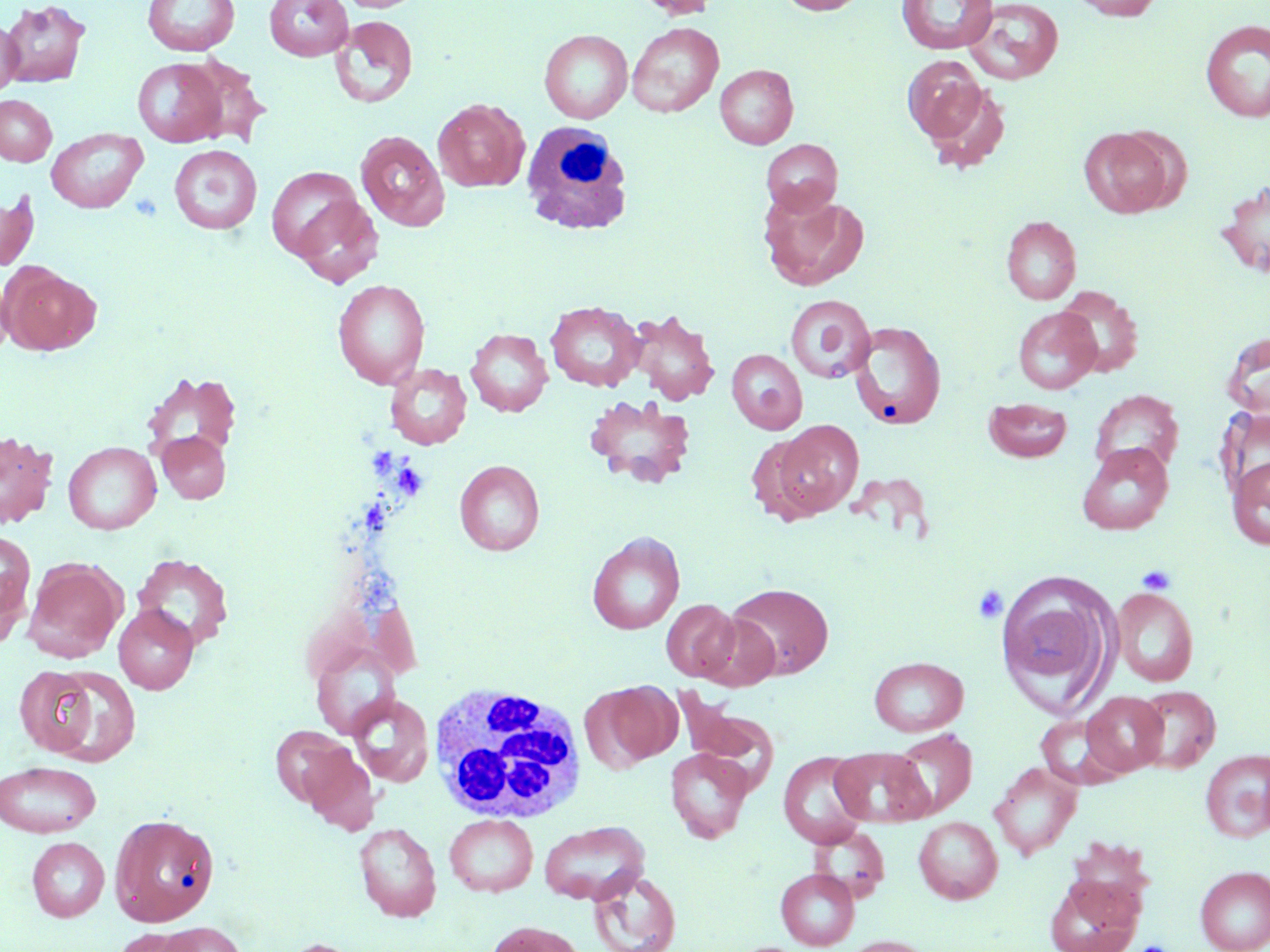
slide-level diagnosis = no evidence of blood parasites
magnification = 1000x
image size = 1270×952 pixels
field of view = single
white blood cell locations = approximate bounding boxes as (x1, y1, x2, y2) in pixels: (520, 121, 635, 236), (429, 685, 588, 826)
platelet locations = approximate bounding boxes as (x1, y1, x2, y2) in pixels: (369, 445, 397, 487), (394, 463, 429, 499), (358, 497, 389, 534), (1137, 565, 1176, 595), (972, 584, 1008, 624), (1135, 940, 1171, 952)
stain = May-Grünwald-Giemsa
preparation = thin blood film
uninfected red blood cell locations = approximate bounding boxes as (x1, y1, x2, y2) in pixels: (2, 0, 91, 87), (142, 0, 239, 56), (264, 0, 353, 61), (336, 0, 424, 12), (633, 0, 719, 20), (777, 0, 869, 15), (896, 0, 998, 54), (1071, 0, 1163, 20), (963, 1, 1064, 85), (329, 15, 418, 108), (0, 18, 21, 98), (1201, 19, 1270, 122), (627, 22, 724, 118), (539, 29, 633, 123), (902, 55, 991, 147), (182, 56, 269, 146), (132, 58, 227, 147), (714, 64, 798, 149), (920, 79, 1012, 174), (0, 94, 56, 166), (433, 98, 529, 192), (46, 128, 147, 213), (1080, 128, 1172, 218), (355, 130, 449, 231), (761, 139, 843, 217), (169, 145, 261, 234), (266, 166, 365, 260), (1217, 181, 1270, 280), (0, 189, 38, 271), (759, 190, 869, 291), (291, 195, 383, 287), (1001, 216, 1082, 305), (3, 264, 101, 356), (0, 278, 13, 361), (332, 279, 429, 388), (1056, 286, 1144, 377), (785, 294, 876, 383), (546, 300, 644, 391), (1013, 307, 1101, 393), (627, 309, 720, 406), (850, 321, 947, 430), (466, 328, 553, 417), (1222, 331, 1270, 419), (726, 349, 807, 434), (385, 363, 472, 449), (140, 369, 242, 468), (1089, 389, 1184, 476), (583, 394, 696, 488), (983, 397, 1072, 463), (774, 420, 863, 516), (0, 431, 59, 528), (157, 431, 230, 503), (747, 434, 826, 524), (62, 441, 161, 534), (1076, 442, 1174, 535), (1228, 456, 1270, 550), (454, 460, 545, 556), (1, 530, 35, 630), (587, 532, 684, 634), (131, 554, 234, 651), (23, 558, 125, 662), (997, 576, 1112, 707), (726, 582, 833, 679), (1111, 587, 1199, 686), (661, 599, 741, 681), (114, 605, 198, 694), (696, 612, 781, 691), (310, 644, 399, 738), (869, 656, 968, 736), (14, 666, 100, 757), (46, 667, 141, 766), (593, 683, 680, 768), (1133, 686, 1220, 773), (674, 688, 778, 787), (1080, 691, 1168, 776), (350, 693, 433, 787), (1036, 715, 1124, 789), (270, 726, 359, 809), (890, 729, 977, 819), (298, 744, 380, 834), (665, 748, 753, 843), (831, 748, 931, 827), (1200, 749, 1270, 843), (778, 752, 870, 847), (0, 760, 102, 838), (989, 761, 1083, 860), (109, 813, 219, 926), (445, 813, 538, 896), (913, 816, 1003, 904), (539, 820, 649, 905), (354, 822, 442, 922), (808, 824, 890, 903), (27, 836, 109, 921), (1195, 866, 1270, 952), (775, 868, 859, 950), (588, 871, 681, 952), (1044, 873, 1143, 952), (154, 921, 246, 952), (485, 921, 585, 952), (111, 928, 198, 952), (841, 935, 935, 952), (277, 938, 368, 952)
modality = light microscopy